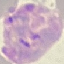

Summary:
  - Result: malaria parasites detected
  - Image type: cell patch, automatically extracted from a larger field of view and resized to 64 × 64 pixels
  - Capture: smartphone camera at the microscope eyepiece
  - Preparation: thin blood film
  - Stain: Giemsa